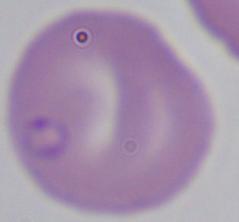

identification = Babesia
modality = micrograph
magnification = 1000x